Assess this cell for malaria.
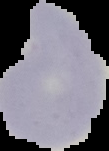

It is uninfected.

{
  "image_size": "109×151 pixels",
  "preparation": "thin blood smear",
  "image_type": "cell region segmented out of the field of view; surrounding area masked to black"
}